Locate every Plasmodium parasite.
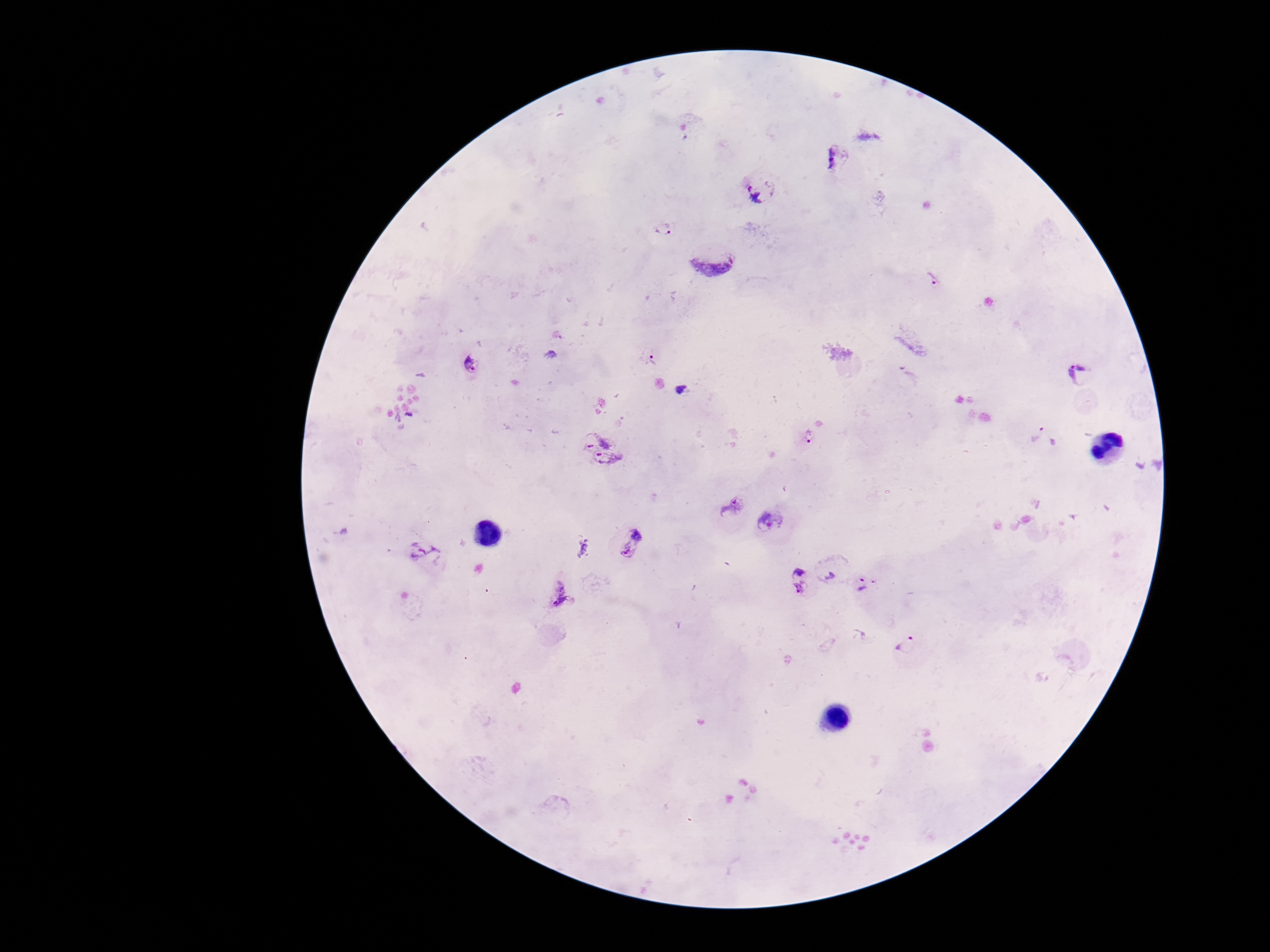
Approximate centers as (x, y) in pixels.
Plasmodium parasites: (838, 158), (761, 189), (664, 231), (717, 257), (932, 275), (650, 355), (472, 365), (1078, 375), (682, 391), (810, 435), (1045, 437), (603, 448), (730, 505), (772, 522), (631, 542), (426, 552), (833, 575), (799, 580), (867, 583), (557, 594), (908, 644).

One field from this slide. Image is 1270×952 pixels. Thick blood smear. 100x magnification. Patient malaria status: infected. Giemsa stain. Smartphone photograph taken through the microscope eyepiece.